Classify this cell by malaria status.
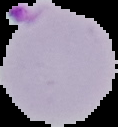
It is parasitized.

{
  "preparation": "thin blood smear",
  "image_type": "cell region segmented out of the field of view; surrounding area masked to black",
  "image_size": "118×127 pixels"
}